Report the malaria status of this cell.
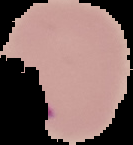

It is parasitized.

Image is 133×145 pixels. From a thin blood film. Cell region segmented out of the field of view; the surrounding area is masked to black.